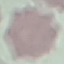 Malaria status: uninfected. Thin smear of blood. Cell patch, automatically extracted from a larger field of view and resized to 64 × 64 pixels. Giemsa stain. Acquired by smartphone through the microscope eyepiece.